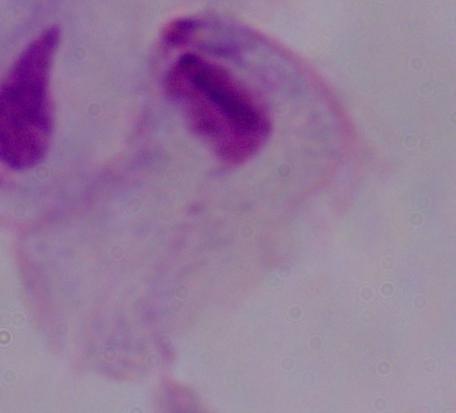
identification = trichomonad
modality = micrograph
magnification = 1000x